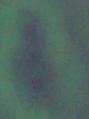
identification: Leishmania
modality: photomicrograph
magnification: 1000x